Describe the morphology of the erythrocytes.
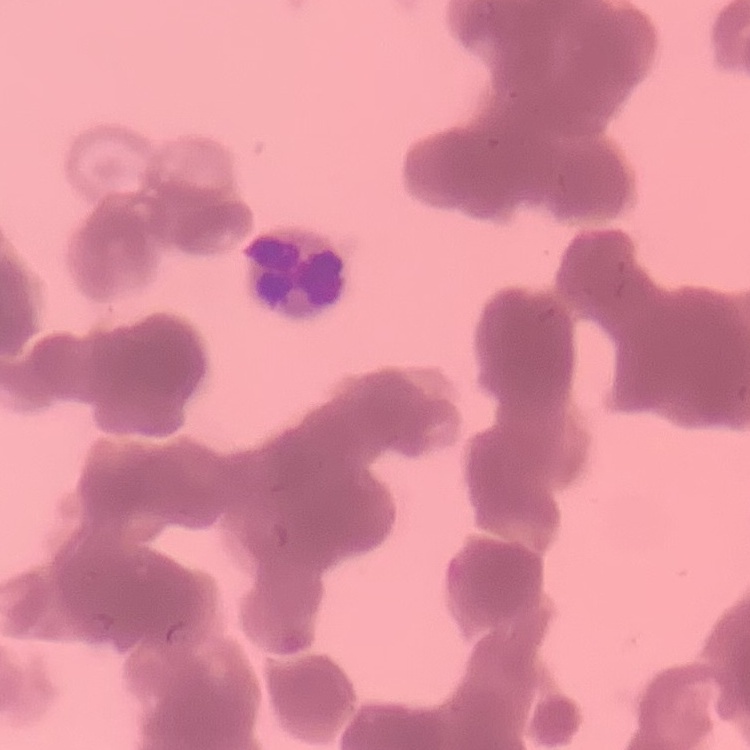
Rouleaux formation.

image type = square crop of a larger photomicrograph
preparation = thin blood smear
stain = Field's or Giemsa